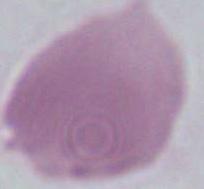

magnification = 1000x
modality = micrograph
identification = erythrocyte